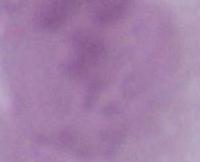
Captured at 1000x magnification. Micrograph. An erythrocyte is seen.